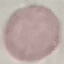

Result: no malaria parasites detected. Cell patch, automatically extracted from a larger field of view and resized to 64 × 64 pixels. Giemsa stain. Photographed with a smartphone camera at the microscope eyepiece. Thin blood film.